Classify this cell by malaria status.
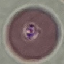

Uninfected.

Cell patch, automatically extracted from a larger field of view and resized to 64 × 64 pixels. Thin blood film. Photographed with a smartphone camera at the microscope eyepiece. Giemsa-stained preparation.